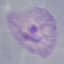
{
  "malaria_status": "parasitized",
  "image_type": "cell patch, automatically extracted from a larger field of view and resized to 64 × 64 pixels",
  "stain": "Giemsa",
  "capture": "smartphone through the microscope eyepiece",
  "preparation": "thin blood film"
}